Identify the parasite.
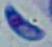
This is Toxoplasma gondii.

modality: micrograph
magnification: 1000x